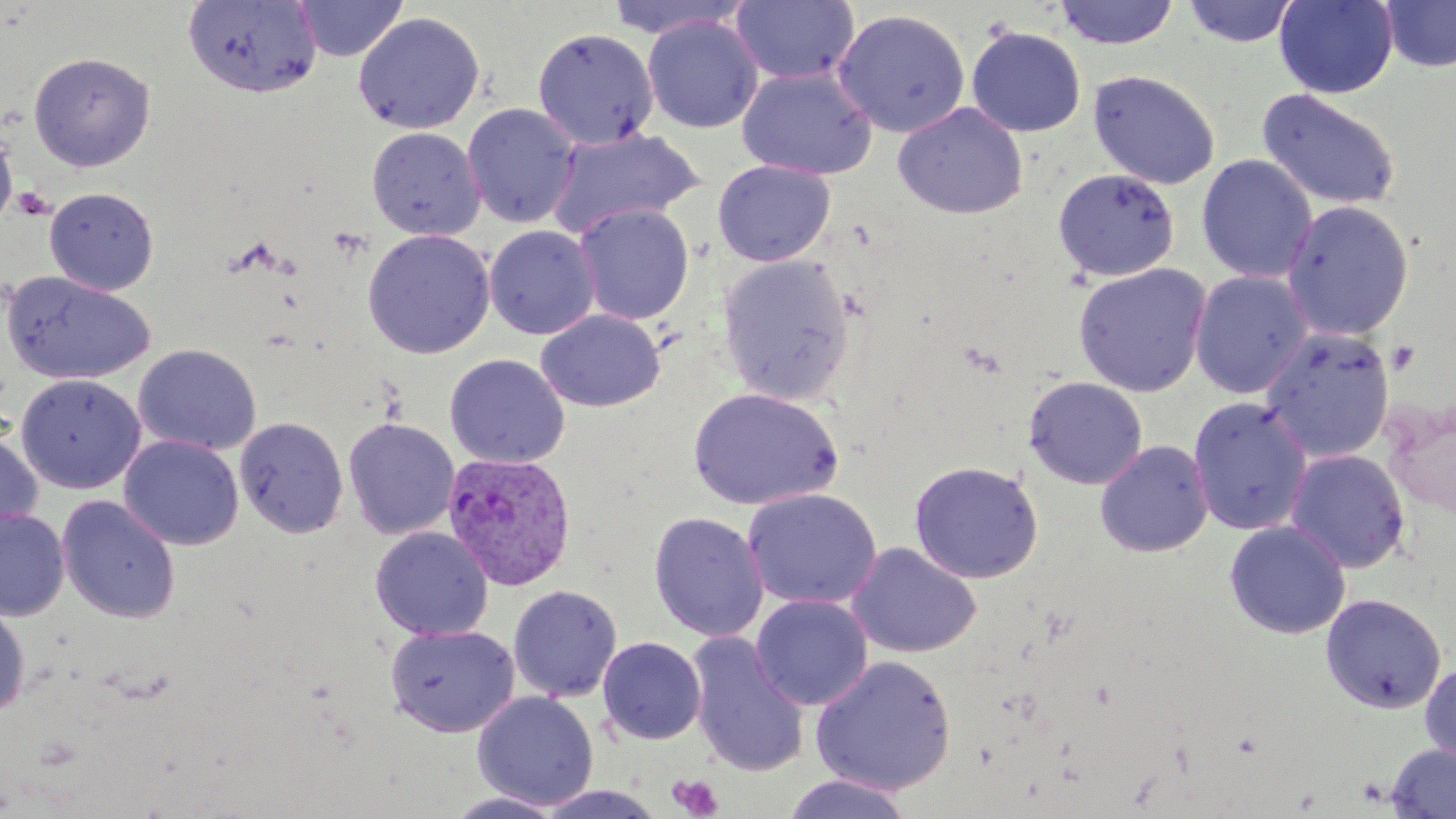

Approximate bounding boxes as named x1/y1/x2/y2 corners in pixels. Uninfected red blood cell locations: (x1=294, y1=0, x2=408, y2=62), (x1=604, y1=0, x2=754, y2=40), (x1=731, y1=0, x2=860, y2=85), (x1=1053, y1=0, x2=1180, y2=49), (x1=1274, y1=0, x2=1398, y2=98), (x1=1381, y1=0, x2=1456, y2=72), (x1=182, y1=1, x2=322, y2=99), (x1=1183, y1=1, x2=1299, y2=48), (x1=833, y1=8, x2=970, y2=138), (x1=353, y1=11, x2=485, y2=134), (x1=642, y1=16, x2=763, y2=133), (x1=533, y1=27, x2=658, y2=150), (x1=966, y1=27, x2=1086, y2=138), (x1=28, y1=51, x2=156, y2=172), (x1=736, y1=66, x2=877, y2=180), (x1=1088, y1=70, x2=1220, y2=190), (x1=1257, y1=88, x2=1402, y2=213), (x1=893, y1=102, x2=1028, y2=220), (x1=462, y1=103, x2=580, y2=228), (x1=1, y1=124, x2=17, y2=230), (x1=367, y1=127, x2=485, y2=240), (x1=545, y1=128, x2=705, y2=238), (x1=1196, y1=154, x2=1317, y2=284), (x1=713, y1=160, x2=835, y2=266), (x1=1052, y1=167, x2=1180, y2=283), (x1=45, y1=187, x2=159, y2=295), (x1=1282, y1=199, x2=1414, y2=341), (x1=573, y1=203, x2=694, y2=325), (x1=484, y1=225, x2=601, y2=339), (x1=362, y1=229, x2=495, y2=359), (x1=717, y1=254, x2=855, y2=405), (x1=1073, y1=263, x2=1211, y2=397), (x1=2, y1=271, x2=155, y2=385), (x1=1189, y1=271, x2=1312, y2=400), (x1=535, y1=309, x2=665, y2=413), (x1=1260, y1=327, x2=1394, y2=463), (x1=133, y1=344, x2=262, y2=455), (x1=445, y1=353, x2=570, y2=468), (x1=15, y1=374, x2=146, y2=494), (x1=1023, y1=376, x2=1148, y2=490), (x1=687, y1=387, x2=843, y2=511), (x1=1188, y1=397, x2=1312, y2=536), (x1=1382, y1=397, x2=1456, y2=519), (x1=234, y1=416, x2=349, y2=538), (x1=343, y1=417, x2=460, y2=541), (x1=0, y1=427, x2=43, y2=539), (x1=119, y1=435, x2=244, y2=551), (x1=1095, y1=440, x2=1215, y2=558), (x1=1285, y1=449, x2=1411, y2=574), (x1=909, y1=460, x2=1044, y2=584), (x1=743, y1=488, x2=881, y2=609), (x1=57, y1=495, x2=181, y2=623), (x1=0, y1=509, x2=70, y2=621), (x1=648, y1=511, x2=768, y2=642), (x1=1224, y1=520, x2=1350, y2=639), (x1=370, y1=526, x2=493, y2=640), (x1=847, y1=542, x2=982, y2=659), (x1=508, y1=585, x2=622, y2=702), (x1=1320, y1=593, x2=1447, y2=713), (x1=751, y1=594, x2=873, y2=711), (x1=0, y1=599, x2=30, y2=718), (x1=384, y1=624, x2=520, y2=736), (x1=687, y1=633, x2=811, y2=777), (x1=598, y1=636, x2=706, y2=744), (x1=810, y1=655, x2=957, y2=795), (x1=1420, y1=661, x2=1456, y2=767), (x1=472, y1=691, x2=598, y2=810), (x1=1385, y1=744, x2=1456, y2=819), (x1=781, y1=773, x2=916, y2=818), (x1=533, y1=785, x2=668, y2=818), (x1=444, y1=790, x2=567, y2=818). Plasmodium vivax-infected red blood cell locations: (x1=442, y1=452, x2=577, y2=591). Platelet locations: (x1=10, y1=186, x2=54, y2=221), (x1=669, y1=773, x2=723, y2=819). Slide-level diagnosis: Plasmodium vivax. Thin blood film. Captured at 1000x magnification. Light microscopy. Image is 1456×819 pixels. May-Grünwald-Giemsa stain. Single field of view.